Name the cell type shown.
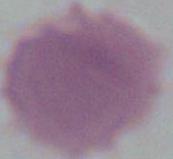
This is an erythrocyte.

magnification: 1000x
modality: photomicrograph